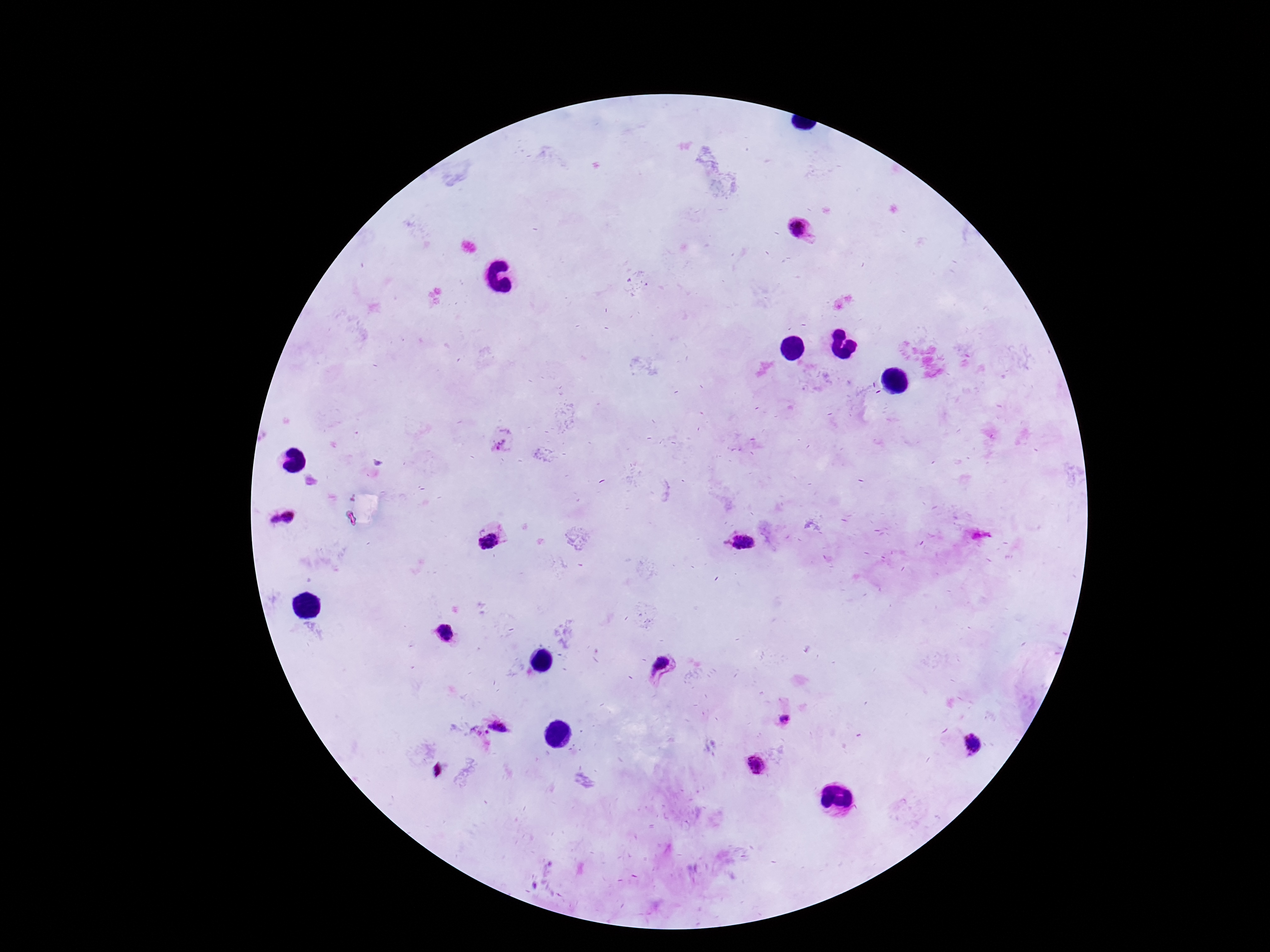 Approximate centers as (x, y) in pixels. Plasmodium parasite locations: (800, 228), (498, 446), (290, 516), (274, 519), (741, 541), (492, 543), (445, 635), (660, 669), (785, 719), (501, 724), (973, 743), (756, 764), (437, 769). Patient malaria status: positive. One field from this slide. Giemsa stain. Thick peripheral-blood smear. Image is 1270×952 pixels. 100x magnification. Photographed through the microscope eyepiece with a smartphone camera.